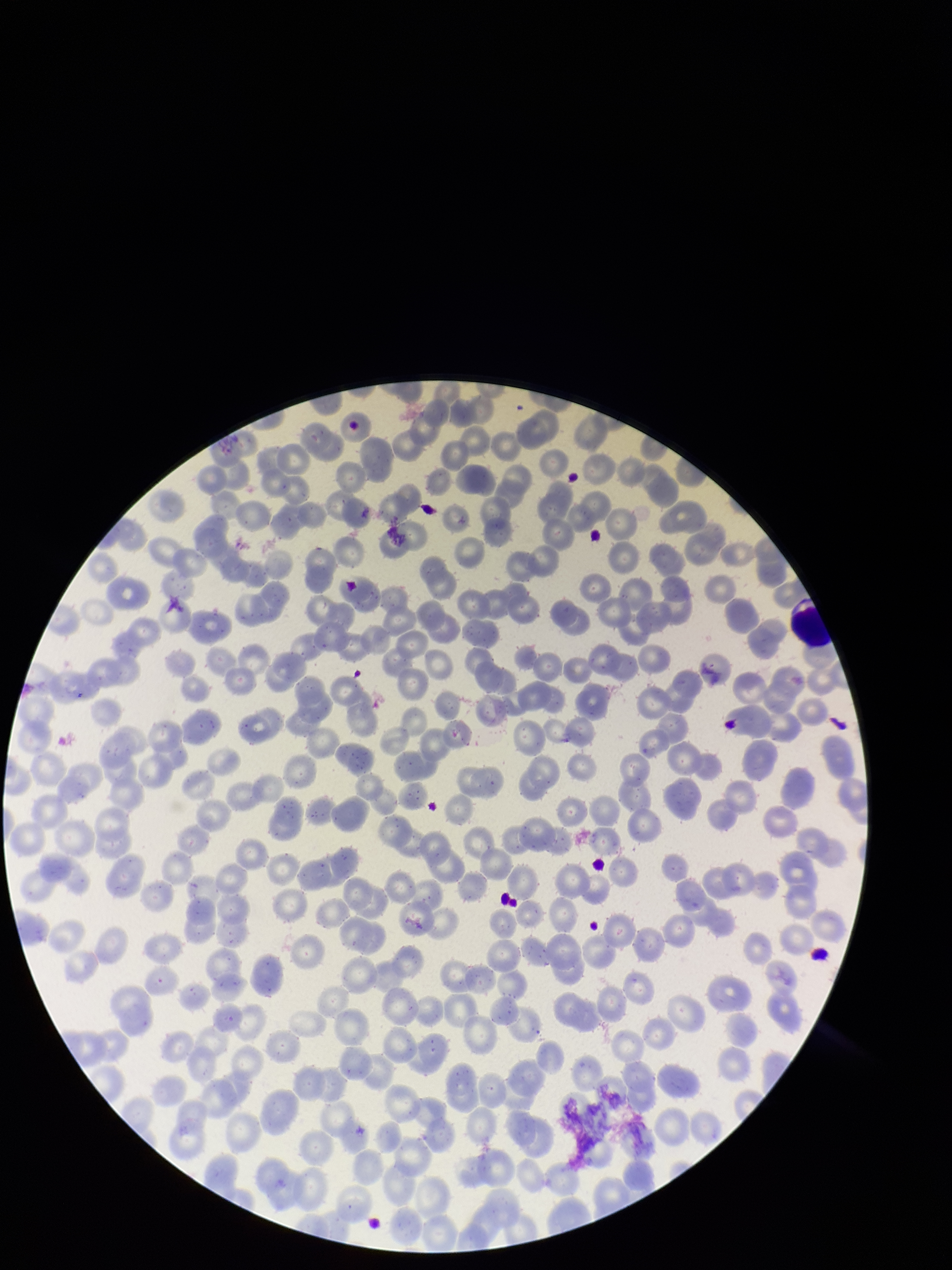
Summary:
  - Parasitized red blood cells: none seen
  - Patient malaria status: infected
  - Parasitized red blood cell count: 0
  - Image size: 952×1270 pixels
  - Red blood cell count: 216
  - Species reported for this patient: Plasmodium vivax
  - Field of view: one from this slide
  - Capture: smartphone photograph through the microscope eyepiece
  - Preparation: thin smear
  - Stain: Giemsa